Describe the morphology of the erythrocytes.
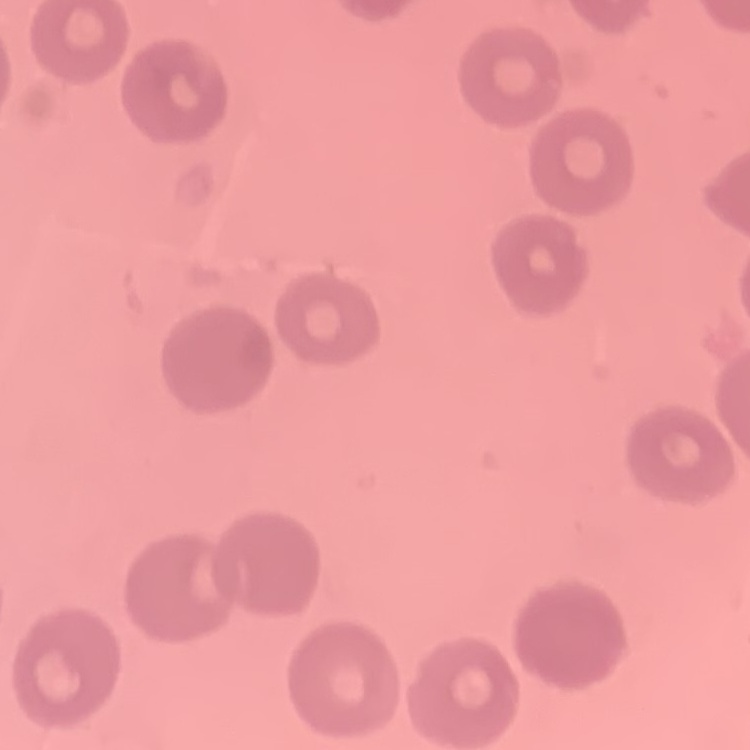
No rouleaux formation.

Square crop of a larger photomicrograph. Thin blood smear. Field's or Giemsa stain.